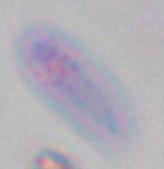

modality: micrograph
magnification: 1000x
identification: Toxoplasma gondii